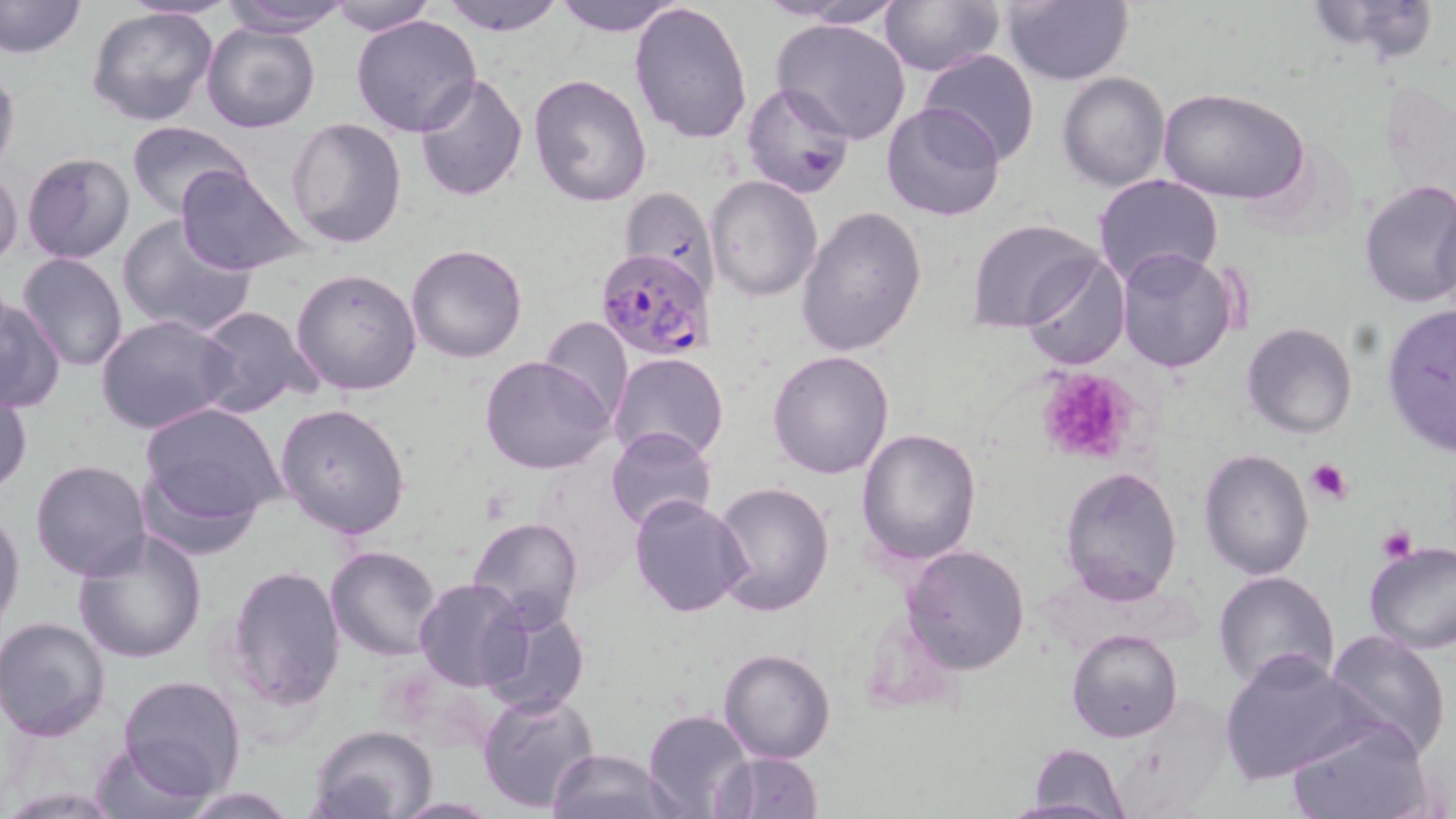

Approximate bounding boxes as (x1,y1)-(x2,y2) corner pairs in pixels. Uninfected red blood cell locations: (0,0)-(86,60), (126,0)-(242,20), (325,0)-(438,35), (436,0)-(570,34), (550,0)-(689,36), (770,0)-(908,28), (878,0)-(1004,75), (1002,0)-(1133,85), (1299,0)-(1442,66), (218,1)-(352,37), (628,2)-(753,145), (86,6)-(221,129), (350,14)-(482,137), (771,17)-(912,146), (201,20)-(321,133), (917,50)-(1040,165), (0,60)-(20,179), (413,72)-(529,203), (1058,72)-(1170,191), (528,75)-(653,208), (742,81)-(854,198), (1159,87)-(1312,205), (879,101)-(1007,223), (286,116)-(408,248), (126,120)-(254,221), (22,152)-(137,264), (173,164)-(310,278), (0,167)-(24,269), (706,174)-(822,301), (1092,174)-(1224,289), (1356,180)-(1456,307), (618,186)-(718,292), (796,206)-(926,356), (116,214)-(257,339), (969,218)-(1102,333), (406,244)-(528,364), (1116,246)-(1240,375), (17,252)-(128,372), (1022,252)-(1130,370), (289,253)-(531,377), (291,268)-(422,395), (0,296)-(66,412), (1381,303)-(1456,459), (196,306)-(324,419), (96,314)-(239,435), (540,317)-(635,428), (1242,322)-(1359,440), (768,351)-(895,479), (609,352)-(729,462), (480,355)-(615,474), (1,384)-(32,496), (139,402)-(286,534), (274,403)-(411,539), (607,426)-(718,534), (856,427)-(981,566), (1199,448)-(1316,580), (30,459)-(151,580), (1060,465)-(1183,603), (712,481)-(836,617), (628,493)-(750,618), (0,505)-(25,635), (468,516)-(584,630), (70,528)-(208,664), (1362,540)-(1456,653), (901,543)-(1031,674), (325,545)-(445,661), (223,564)-(347,713), (1212,570)-(1342,695), (413,578)-(530,691), (480,603)-(589,717), (1,616)-(114,741), (1065,628)-(1184,743), (1323,629)-(1453,759), (718,647)-(837,764), (1219,651)-(1376,786), (117,674)-(249,800), (654,683)-(830,810), (478,690)-(600,811), (642,709)-(757,818), (1285,714)-(1435,819), (310,726)-(440,818), (89,738)-(218,819), (1025,743)-(1133,815), (544,747)-(680,819), (719,751)-(824,819), (178,785)-(299,817), (1004,798)-(1128,819), (390,799)-(505,818). Platelet locations: (1037,367)-(1139,465), (1306,458)-(1354,505), (1377,524)-(1419,561). Plasmodium falciparum-infected red blood cell locations: (593,246)-(713,361). Slide-level diagnosis: Plasmodium falciparum. Image is 1456×819 pixels. Optical microscopy. May-Grünwald-Giemsa-stained preparation. Thin blood smear. Single field of view. Captured at 1000x magnification.